Describe the morphology of the red blood cells.
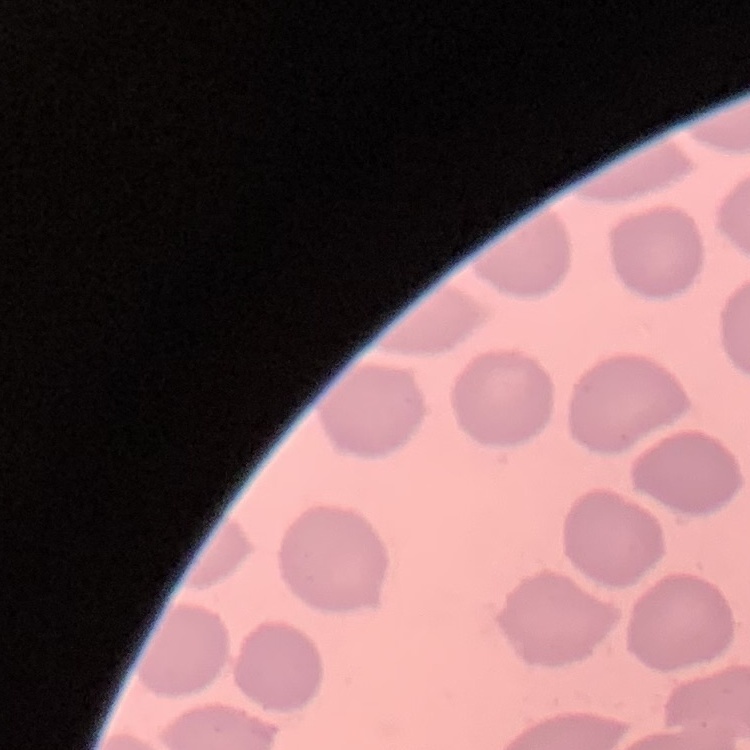
They show no rouleaux formation.

image type = square crop of a larger photomicrograph
stain = Field's or Giemsa
preparation = thin blood smear